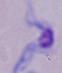

Summary:
  - Identification: trypanosome
  - Modality: photomicrograph
  - Magnification: 1000x